Identify the blood parasite species.
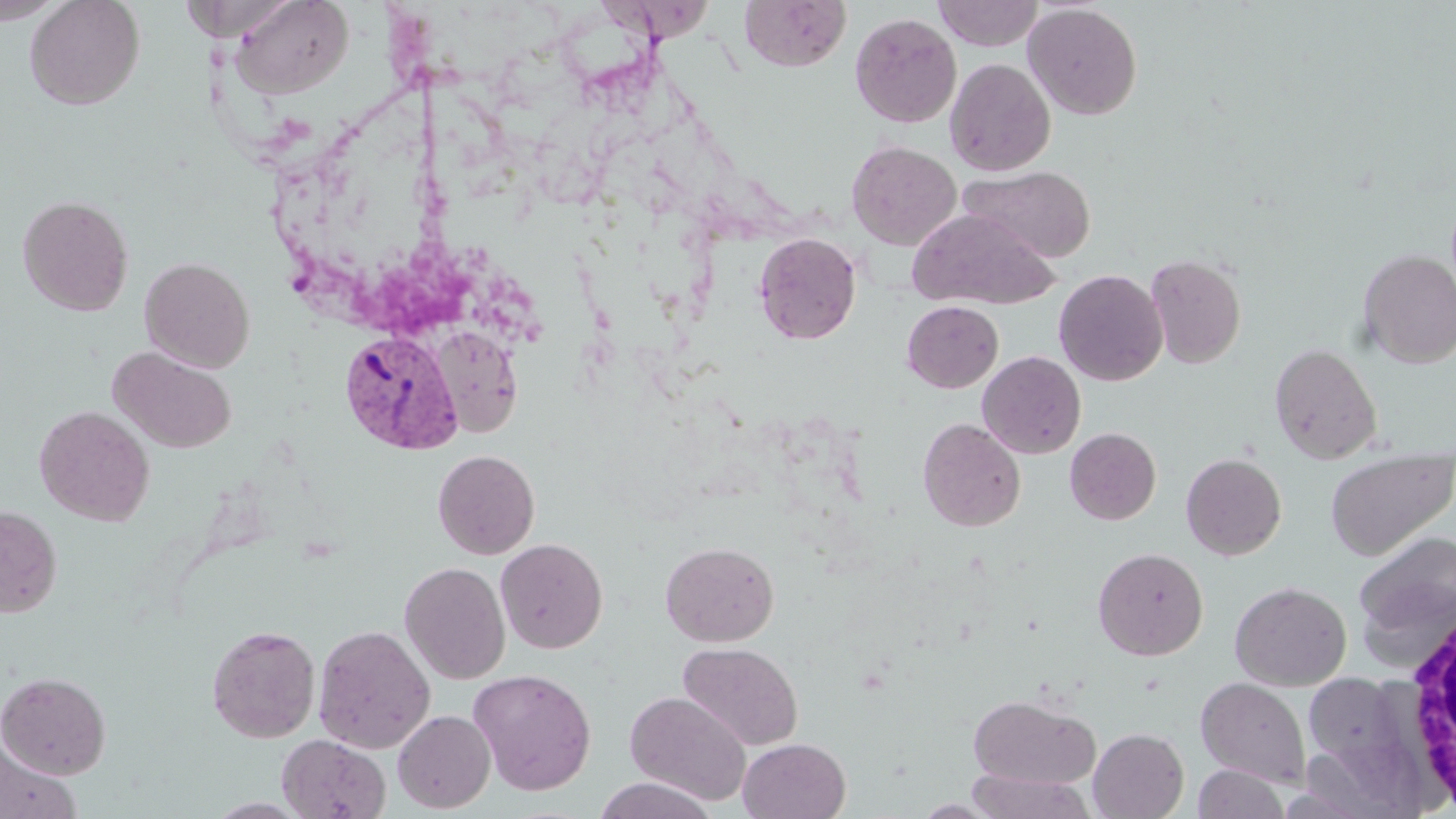

Plasmodium vivax.

image size = 1456×819 pixels
Plasmodium vivax-infected red blood cell locations = approximate bounding boxes as [x1, y1, x2, y2] in pixels: [339, 329, 462, 453]
preparation = thin blood film
uninfected red blood cell locations = approximate bounding boxes as [x1, y1, x2, y2] in pixels: [0, 0, 69, 25], [24, 0, 146, 110], [230, 0, 354, 99], [739, 0, 850, 72], [933, 0, 1044, 50], [1023, 3, 1142, 120], [850, 13, 962, 128], [945, 57, 1056, 176], [846, 141, 962, 250], [959, 165, 1096, 263], [17, 195, 134, 317], [906, 209, 1057, 310], [753, 232, 861, 344], [1357, 248, 1456, 368], [1145, 254, 1246, 369], [139, 256, 255, 372], [1053, 269, 1168, 386], [902, 300, 1004, 392], [427, 326, 524, 438], [1268, 343, 1383, 464], [109, 346, 237, 454], [977, 351, 1086, 458], [33, 404, 155, 526], [917, 417, 1026, 531], [1065, 428, 1160, 525], [1325, 447, 1455, 561], [432, 449, 540, 559], [1181, 452, 1287, 560], [0, 505, 62, 617], [1354, 530, 1455, 649], [495, 538, 608, 653], [660, 541, 779, 646], [1093, 547, 1209, 660], [399, 561, 511, 684], [1229, 581, 1351, 690], [206, 624, 321, 742], [313, 624, 435, 753], [678, 642, 804, 751], [468, 668, 597, 795], [1307, 668, 1420, 816], [0, 671, 111, 779], [1195, 676, 1312, 788], [625, 691, 752, 805], [967, 693, 1101, 789], [392, 710, 496, 813], [1088, 728, 1189, 818], [276, 734, 391, 819], [738, 738, 850, 819], [0, 739, 81, 819], [1194, 764, 1291, 819], [964, 770, 1097, 818], [593, 776, 718, 819]
magnification = 1000x
stain = May-Grünwald-Giemsa
white blood cell locations = approximate bounding boxes as [x1, y1, x2, y2] in pixels: [1395, 596, 1456, 809]
modality = optical microscopy
field of view = one of a larger specimen